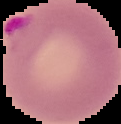 From a thin blood film. Malaria status: parasitized. Image is 121×124 pixels. Segmented cell region on a black background.